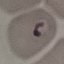

malaria status = parasitized
image type = automatically extracted cell patch, resized to 64 × 64 pixels
preparation = thin blood film
capture = smartphone through the microscope eyepiece
stain = Giemsa